State which parasite is depicted.
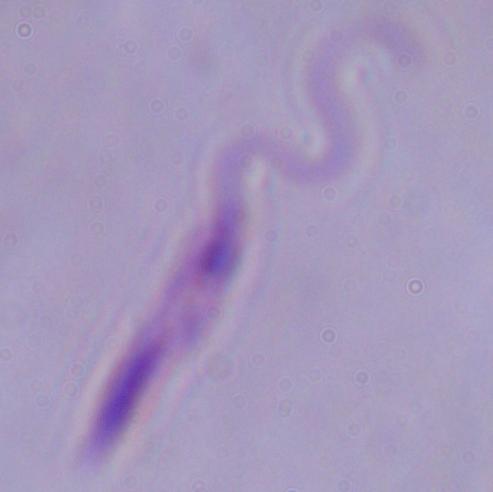
This is Leishmania.

Micrograph. 1000x magnification.